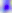
{
  "identification": "Toxoplasma gondii",
  "magnification": "400x",
  "modality": "photomicrograph"
}